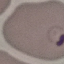
Malaria status: parasitized. Thin blood film. Acquired by smartphone through the microscope eyepiece. Automatically extracted cell patch, resized to 64 × 64 pixels. Giemsa-stained preparation.